Report the malaria status of this cell.
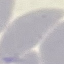
Uninfected.

{
  "image_type": "automatically extracted cell patch, resized to 64 × 64 pixels",
  "capture": "smartphone camera at the microscope eyepiece",
  "stain": "Giemsa",
  "preparation": "thin blood film"
}